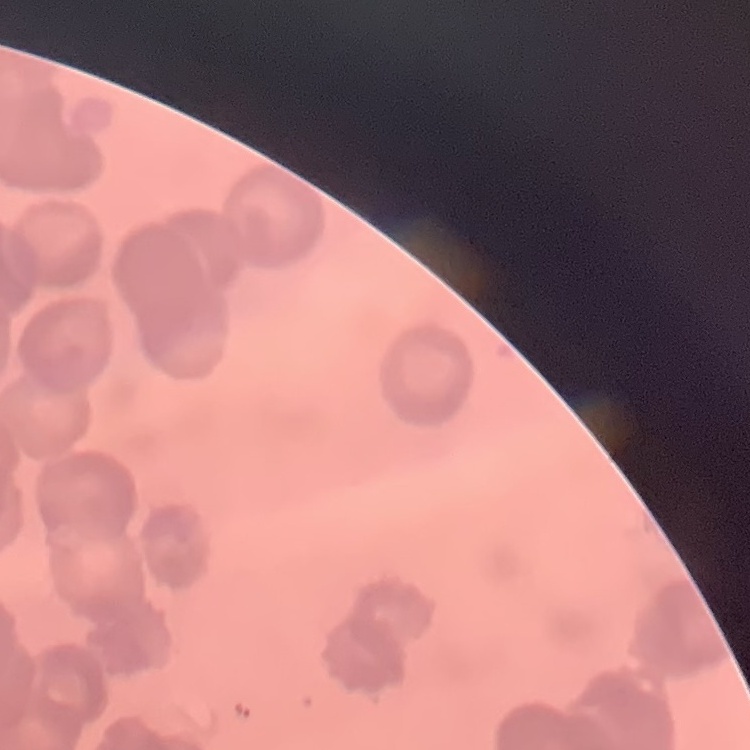
Summary:
  - Red blood cell morphology: rouleaux formation
  - Stain: Field's or Giemsa
  - Preparation: thin blood smear
  - Image type: one tile cut from a larger photomicrograph